Assess this cell for malaria.
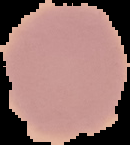

It is uninfected.

Image is 130×145 pixels. From a thin blood smear. Segmented cell region on a black background.